Report the malaria status of this cell.
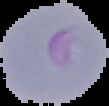

It is parasitized.

image size = 109×106 pixels
preparation = thin blood smear
image type = cell region segmented out of the field of view; surrounding area masked to black